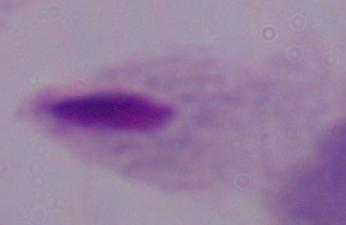

Micrograph. Captured at 1000x magnification. A trichomonad is seen.